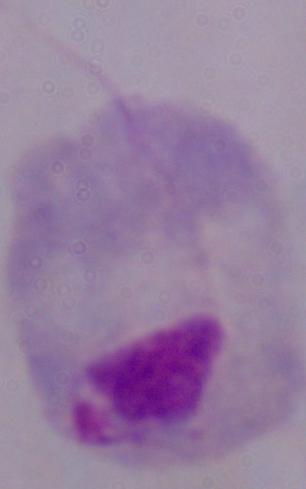

Captured at 1000x magnification. A trichomonad is shown. Photomicrograph.